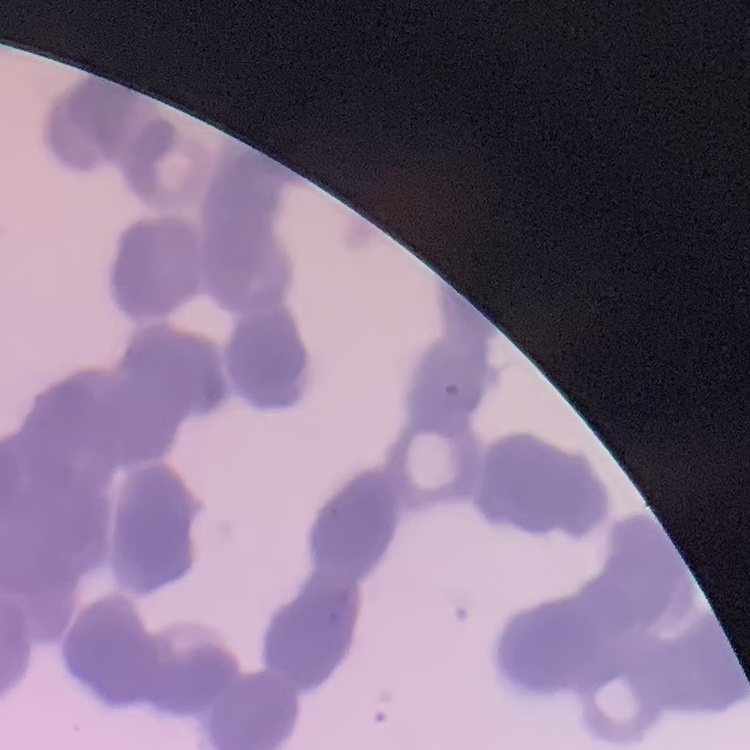

Summary:
  - Erythrocyte morphology: rouleaux formation
  - Preparation: thin peripheral smear
  - Image type: one tile cut from a larger photomicrograph
  - Stain: Field's or Giemsa